Name the parasite shown.
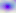

This is Toxoplasma gondii.

modality = micrograph
magnification = 400x